Classify this cell by malaria status.
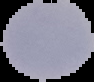
Uninfected.

image size = 94×82 pixels
preparation = thin blood smear
image type = segmented cell region on a black background